Comment on the morphology of the erythrocytes.
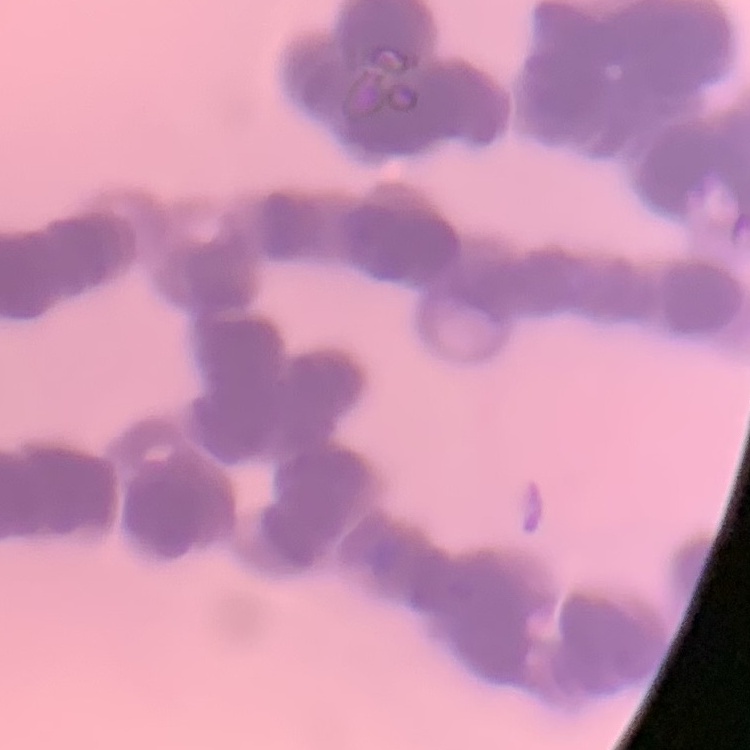
Rouleaux formation.

{
  "image_type": "one tile cut from a larger photomicrograph",
  "preparation": "thin blood smear",
  "stain": "Field's or Giemsa"
}